Comment on the morphology of the red blood cells.
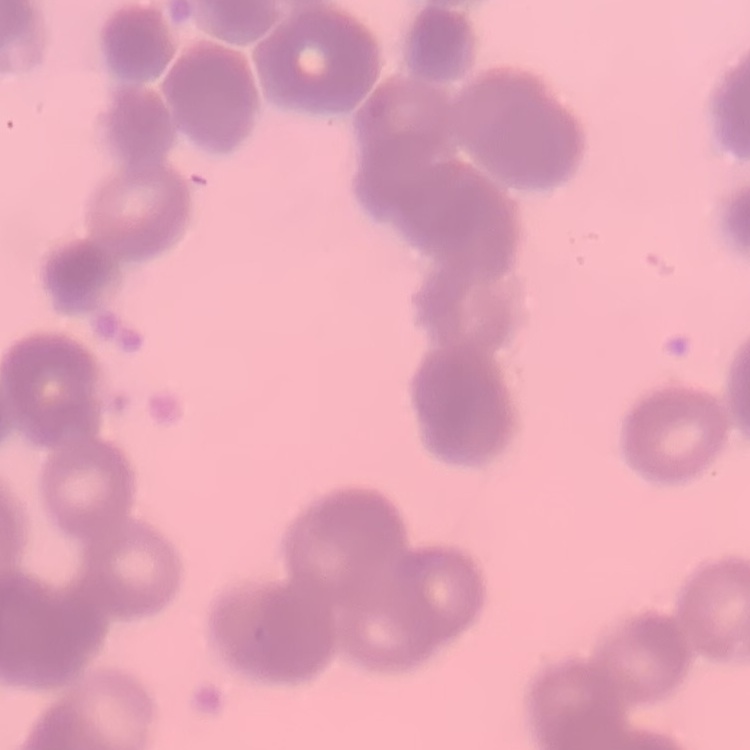
Rouleaux formation.

Field's or Giemsa stain. Square crop of a larger photomicrograph. Thin blood film.